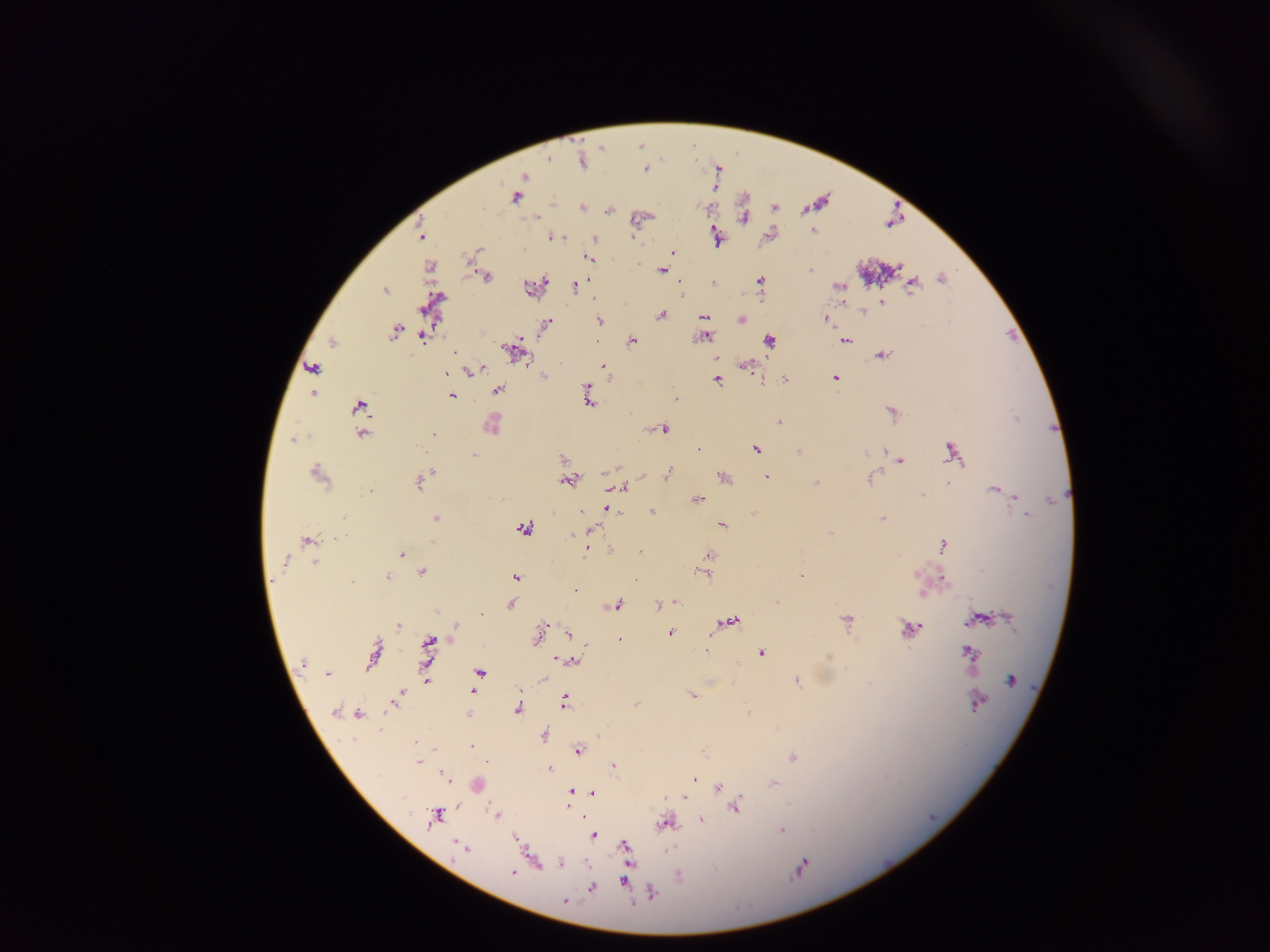
capture = mobile-phone photograph through a microscope
malaria parasite locations = approximate centers as [x, y] in pixels: [550, 159], [582, 162], [646, 169], [524, 177], [515, 197], [582, 208], [775, 208], [609, 211], [537, 218], [744, 218], [813, 231], [421, 236], [552, 237], [716, 237], [595, 238], [478, 250], [673, 253], [588, 257], [661, 270], [811, 271], [487, 277], [941, 278], [759, 280], [713, 284], [575, 286], [838, 286], [912, 286], [531, 289], [384, 291], [882, 302], [863, 311], [660, 315], [704, 317], [742, 319], [827, 319], [599, 321], [547, 323], [394, 332], [423, 337], [705, 337], [520, 340], [768, 340], [845, 340], [332, 342], [633, 342], [506, 348], [513, 350], [454, 352], [882, 355], [716, 358], [523, 359], [746, 366], [603, 368], [312, 369], [477, 369], [447, 374], [544, 378], [835, 378], [785, 379], [717, 380], [497, 389], [313, 394], [451, 396], [676, 398], [588, 399], [360, 406], [892, 413], [1017, 418], [779, 422], [491, 425], [361, 426], [664, 429], [362, 433], [433, 434], [293, 440], [698, 449], [757, 450], [884, 450], [798, 452], [865, 453], [952, 453], [474, 455], [563, 460], [901, 461], [431, 470], [605, 472], [667, 474], [318, 475], [724, 477], [767, 477], [868, 478], [419, 482], [567, 482], [816, 482], [947, 483], [619, 488], [993, 490], [369, 491], [922, 495], [1015, 496], [501, 499], [698, 499], [609, 509], [653, 512], [1026, 515], [343, 517], [436, 518], [883, 518], [722, 525], [523, 529], [590, 529], [830, 532], [338, 538], [307, 541], [943, 545], [586, 551], [401, 554], [709, 555], [286, 562], [314, 563], [422, 573], [702, 574], [388, 576], [802, 576], [515, 577], [943, 577], [635, 580], [352, 582], [575, 589], [922, 595], [676, 602], [777, 602], [511, 605], [616, 605], [660, 605], [436, 611], [1009, 618], [846, 620], [977, 620], [731, 621], [969, 621], [456, 625], [398, 626], [910, 628], [670, 633], [539, 634], [569, 634], [619, 640], [430, 644], [706, 650], [760, 653], [969, 653], [373, 655], [571, 661], [303, 663], [480, 673], [328, 674], [543, 679], [426, 680], [1011, 680], [797, 683], [472, 691], [399, 695], [691, 695], [396, 698], [565, 702], [978, 704], [635, 705], [518, 709], [335, 712], [748, 712], [359, 714], [544, 735], [471, 746], [578, 751], [793, 757], [418, 762], [486, 763], [614, 765], [550, 769], [442, 775], [694, 779], [774, 784], [718, 786], [570, 792], [592, 793], [684, 799], [568, 807], [736, 807], [496, 815], [434, 817], [701, 819], [666, 823], [782, 831], [593, 835], [456, 845], [461, 847], [625, 847], [561, 863], [801, 868], [512, 872], [679, 876], [623, 881], [592, 887], [652, 894], [565, 901]
country = Ghana
image size = 1270×952 pixels
preparation = thick blood smear
field of view = single